Point out each Plasmodium parasite and classify it by life-cycle stage.
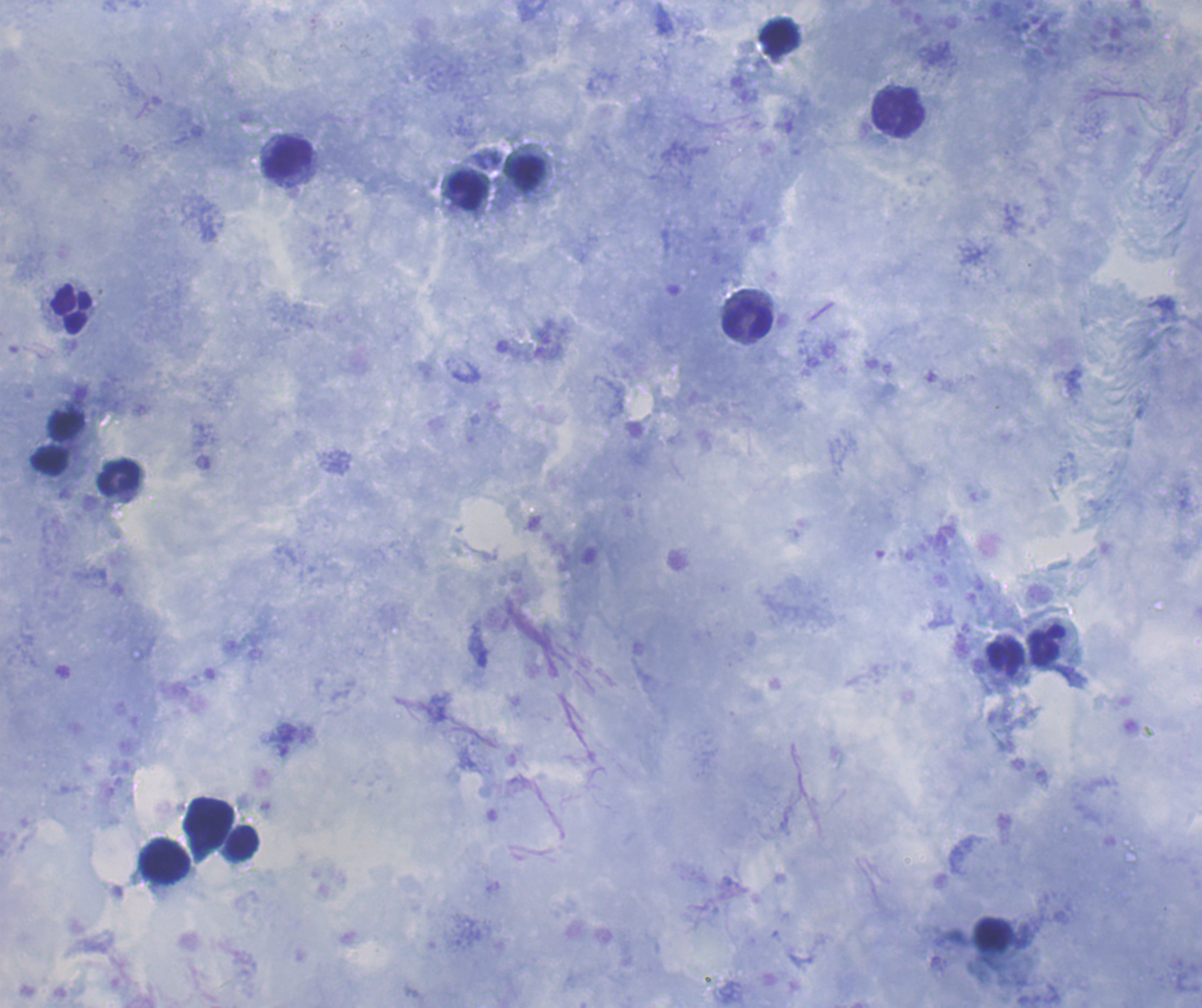
No Plasmodium parasites seen.

Approximate object centers, in pixels from the top-left corner. Leukocyte locations: (x=780, y=37), (x=899, y=112), (x=288, y=158), (x=527, y=174), (x=468, y=191), (x=71, y=309), (x=747, y=321), (x=67, y=425), (x=51, y=460), (x=119, y=478), (x=1045, y=646), (x=1005, y=657), (x=209, y=822), (x=242, y=843), (x=165, y=861). One field from this slide. Background quality: good. 100x magnification. Previously used in an actual diagnosis. Coloration quality: good. Thick blood smear. Romanowsky-stained preparation. Image is 1202×1008 pixels.